Report the malaria status of this cell.
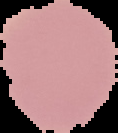

It is uninfected.

Summary:
  - Image type: segmented cell region with the area outside set to black
  - Image size: 118×133 pixels
  - Preparation: thin blood film